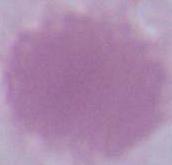
{
  "magnification": "1000x",
  "modality": "photomicrograph",
  "identification": "red blood cell"
}